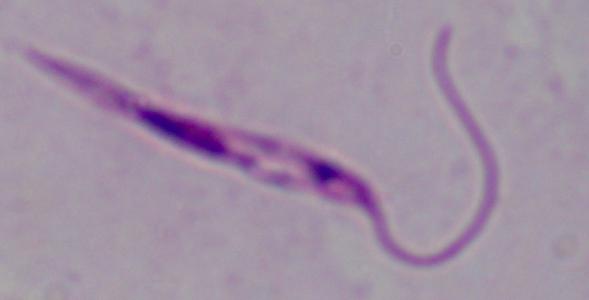
Summary:
  - Modality: micrograph
  - Identification: Leishmania
  - Magnification: 1000x